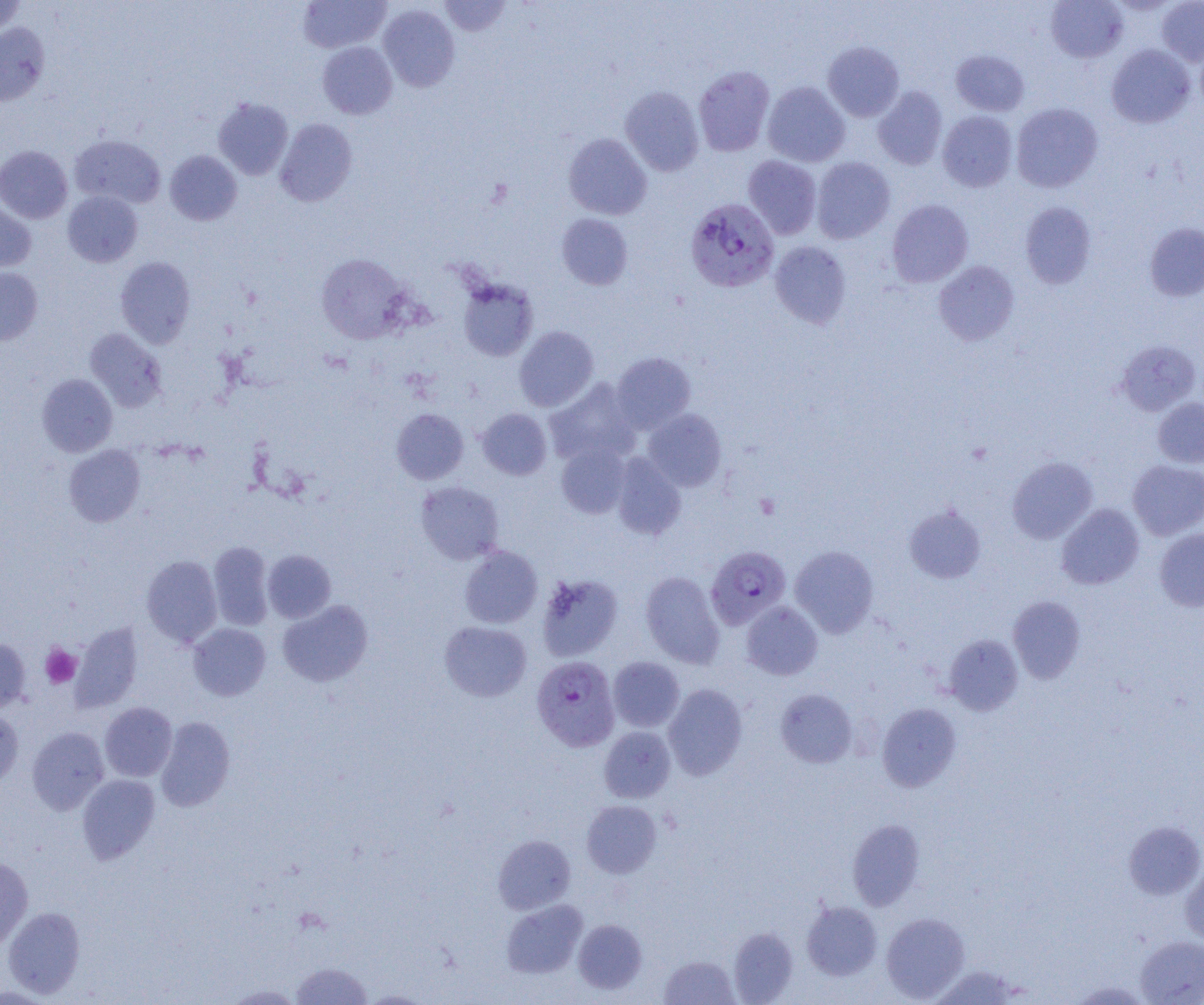

Approximate bounding boxes as (x1, y1, x2, y2) in pixels. Uninfected red blood cell locations: (298, 0, 390, 53), (439, 0, 511, 36), (1045, 0, 1128, 63), (1156, 0, 1204, 66), (0, 1, 27, 37), (299, 2, 460, 73), (378, 4, 459, 91), (0, 22, 49, 106), (822, 41, 904, 121), (318, 42, 397, 119), (1106, 44, 1195, 128), (951, 50, 1029, 116), (693, 65, 775, 156), (763, 81, 850, 167), (873, 86, 947, 169), (620, 87, 704, 176), (213, 98, 293, 180), (1011, 103, 1103, 192), (937, 111, 1017, 192), (274, 119, 357, 207), (563, 133, 652, 220), (70, 135, 165, 208), (0, 145, 72, 223), (165, 150, 242, 225), (742, 155, 821, 239), (811, 157, 895, 244), (63, 191, 143, 267), (0, 198, 36, 273), (887, 199, 973, 287), (1020, 202, 1096, 288), (557, 213, 633, 290), (1144, 223, 1204, 301), (770, 241, 852, 328), (316, 253, 413, 344), (115, 256, 196, 348), (933, 261, 1019, 345), (0, 267, 43, 346), (457, 277, 539, 361), (514, 326, 598, 411), (85, 328, 167, 412), (1116, 339, 1201, 416), (612, 352, 696, 433), (37, 373, 117, 456), (544, 378, 641, 467), (1152, 397, 1204, 468), (391, 408, 469, 485), (477, 408, 552, 480), (642, 409, 726, 491), (557, 442, 632, 519), (63, 444, 145, 527), (611, 453, 686, 540), (1007, 456, 1097, 543), (1128, 460, 1204, 540), (415, 481, 504, 565), (1057, 504, 1144, 589), (904, 505, 986, 584), (1155, 528, 1204, 611), (208, 541, 274, 630), (459, 545, 543, 628), (790, 545, 879, 637), (262, 549, 336, 622), (141, 555, 222, 647), (640, 571, 725, 668), (537, 573, 623, 661), (1008, 596, 1085, 683), (278, 600, 373, 687), (741, 601, 823, 680), (439, 621, 532, 702), (70, 623, 143, 712), (188, 623, 270, 701), (944, 635, 1023, 715), (0, 639, 31, 712), (608, 656, 685, 732), (663, 683, 748, 780), (775, 689, 857, 768), (100, 702, 177, 781), (877, 703, 961, 791), (0, 707, 23, 788), (155, 716, 236, 811), (27, 727, 109, 814), (599, 727, 675, 802), (77, 774, 160, 864), (581, 800, 661, 878), (848, 819, 925, 910), (1124, 821, 1204, 899), (493, 834, 576, 914), (0, 857, 33, 951), (1180, 862, 1204, 945), (501, 899, 588, 978), (802, 901, 882, 980), (3, 907, 86, 998), (881, 912, 970, 1002), (573, 919, 647, 994), (728, 926, 798, 1004), (1136, 935, 1204, 1004), (659, 955, 739, 1004), (291, 961, 373, 1004), (1069, 981, 1153, 1004), (223, 983, 304, 1004), (359, 990, 432, 1004). Platelet locations: (755, 493, 781, 519), (40, 644, 81, 688). Plasmodium falciparum-infected red blood cell locations: (685, 198, 780, 293), (705, 546, 791, 629), (531, 655, 620, 752). Slide-level diagnosis: Plasmodium falciparum. Single field of view. Optical microscopy. 1000x magnification. Image is 1204×1005 pixels. Thin blood film.